Locate every malaria parasite.
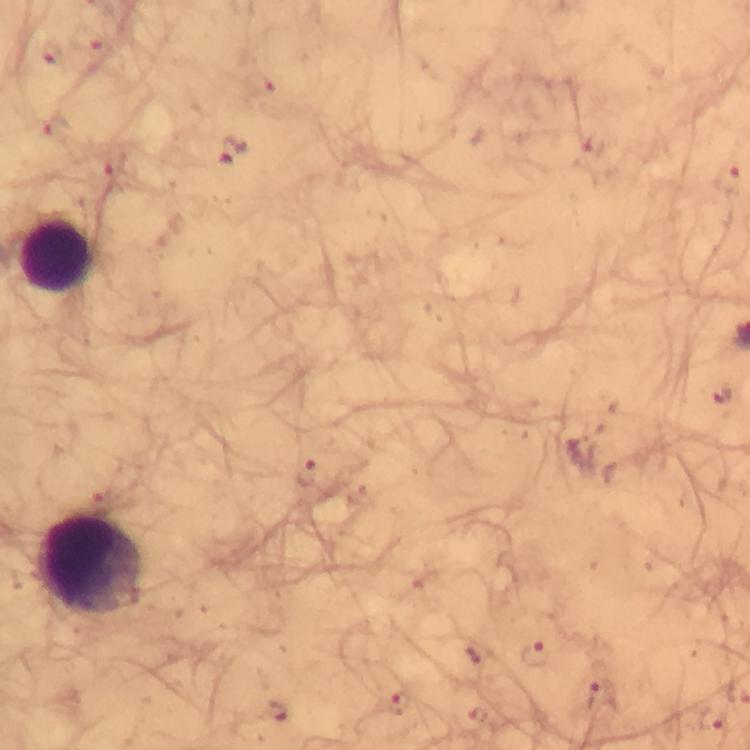
Approximate centers as [x, y] in pixels.
Malaria parasites: [91, 41], [53, 57], [259, 83], [231, 152], [116, 167], [729, 182], [723, 397], [306, 475], [534, 653], [601, 695], [398, 704], [275, 713], [709, 721].

{
  "immersion_oil": "used",
  "leukocyte_locations": "approximate centers as [x, y] in pixels: [56, 255], [89, 566]",
  "magnification": "100x",
  "image_size": "750×750 pixels",
  "preparation": "thick smear",
  "capture": "smartphone camera through the microscope",
  "context": "from a diagnostic examination for malaria",
  "stain": "Giemsa",
  "cropped_from": "a single field of view"
}